State the preparation type.
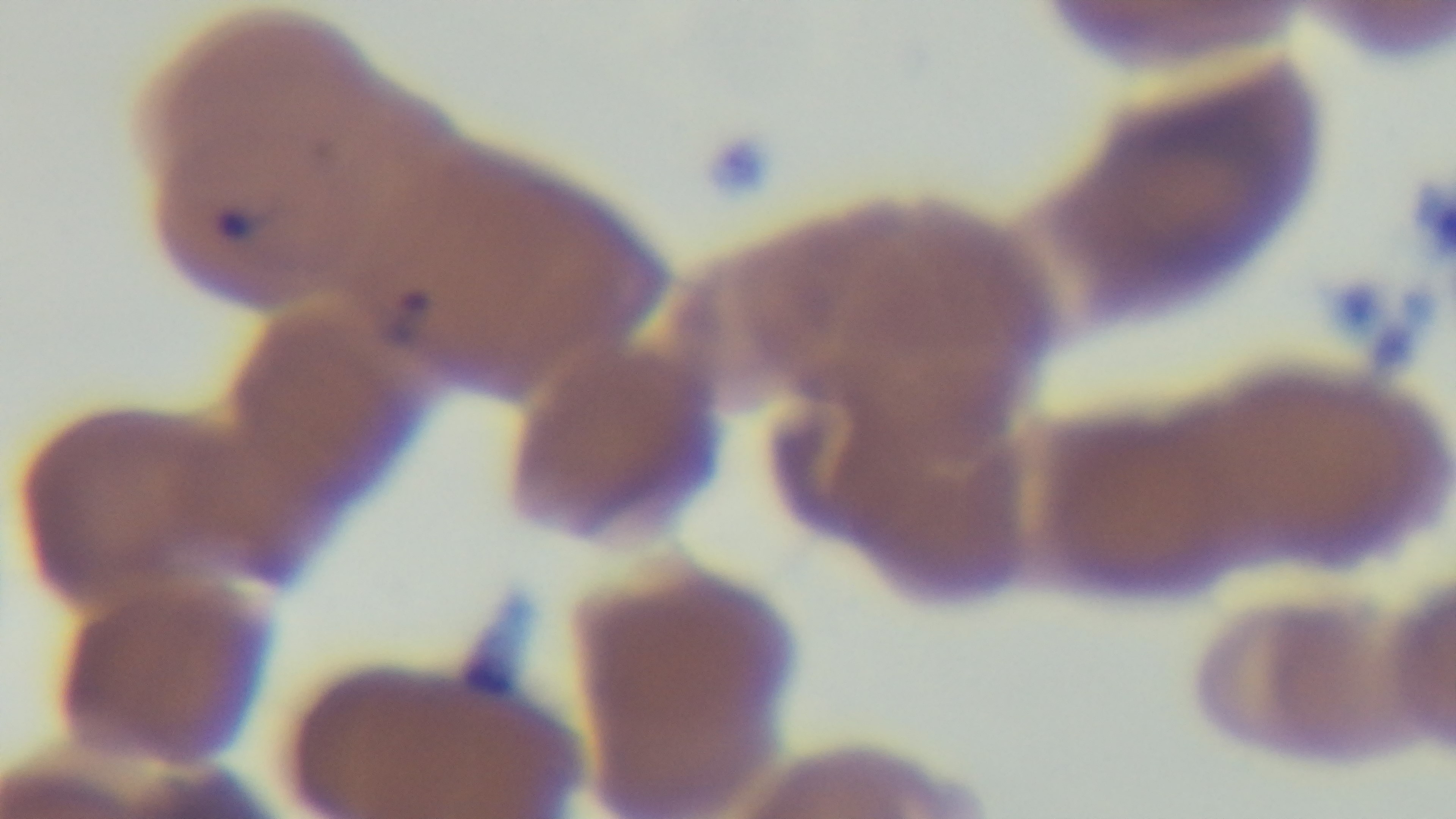

A thin smear.

{
  "field_of_view": "single",
  "stain": "Giemsa",
  "malaria_status": "infected",
  "modality": "light microscopy",
  "objective": "100x oil immersion",
  "capture": "mounted 4K digital camera"
}